Give the extent of all Plasmodium falciparum-infected red blood cells.
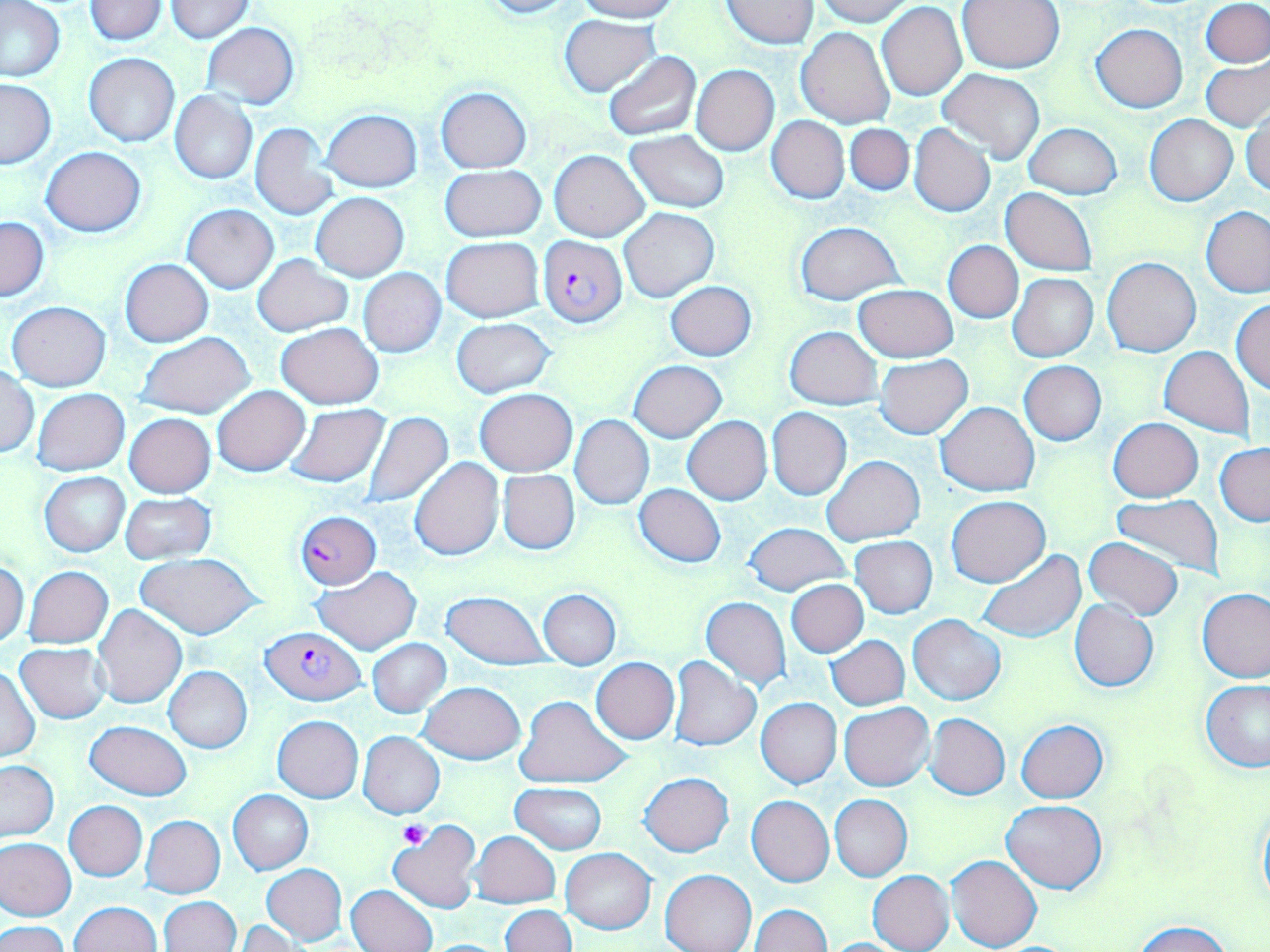
Approximate bounding boxes as (x1, y1, x2, y2) in pixels.
Plasmodium falciparum-infected red blood cells: (537, 234, 626, 327), (295, 511, 379, 588), (261, 626, 365, 705).

Platelet locations: (398, 821, 429, 848). Uninfected red blood cell locations: (0, 0, 68, 83), (475, 0, 584, 19), (575, 0, 681, 22), (815, 0, 917, 26), (84, 1, 166, 44), (721, 1, 818, 49), (957, 1, 1065, 74), (1202, 1, 1269, 66), (164, 2, 254, 43), (878, 3, 967, 100), (560, 15, 658, 95), (201, 22, 299, 109), (1090, 22, 1188, 113), (796, 26, 896, 128), (602, 51, 701, 140), (84, 53, 179, 147), (1202, 59, 1270, 132), (690, 65, 779, 155), (937, 68, 1045, 164), (0, 78, 56, 168), (436, 86, 532, 172), (169, 91, 257, 184), (322, 108, 422, 193), (1243, 108, 1270, 199), (1145, 114, 1237, 205), (768, 115, 849, 203), (250, 123, 340, 219), (845, 123, 914, 195), (909, 123, 995, 218), (1023, 123, 1122, 199), (624, 131, 730, 211), (40, 146, 147, 236), (549, 148, 649, 241), (440, 166, 545, 243), (1002, 188, 1097, 275), (311, 193, 408, 281), (183, 204, 278, 293), (1202, 207, 1269, 296), (619, 208, 718, 301), (1, 217, 48, 301), (794, 221, 905, 304), (441, 237, 545, 323), (943, 241, 1023, 323), (253, 254, 352, 336), (1102, 256, 1200, 357), (120, 258, 213, 345), (358, 269, 447, 357), (1007, 273, 1098, 362), (665, 281, 756, 360), (853, 283, 958, 362), (800, 297, 954, 385), (1231, 299, 1270, 394), (7, 302, 111, 390), (450, 317, 557, 399), (277, 323, 383, 409), (785, 327, 882, 408), (136, 331, 256, 420), (1160, 346, 1255, 438), (875, 355, 973, 439), (630, 359, 726, 442), (1020, 360, 1107, 445), (1, 366, 40, 458), (212, 386, 309, 475), (32, 388, 129, 475), (475, 389, 576, 476), (936, 400, 1039, 496), (284, 403, 390, 487), (767, 407, 852, 501), (362, 411, 454, 507), (125, 413, 216, 497), (570, 415, 654, 509), (682, 416, 771, 504), (1108, 417, 1203, 502), (1215, 443, 1270, 525), (821, 455, 924, 547), (409, 457, 503, 561), (497, 470, 579, 555), (39, 472, 129, 556), (634, 484, 726, 567), (120, 492, 216, 564), (1110, 495, 1224, 578), (947, 496, 1049, 587), (744, 522, 850, 597), (851, 536, 937, 618), (1084, 536, 1183, 620), (977, 548, 1085, 643), (138, 554, 262, 640), (0, 560, 27, 647), (23, 566, 112, 649), (311, 566, 420, 654), (786, 580, 868, 657), (1198, 589, 1270, 684), (538, 590, 620, 669), (439, 591, 553, 670), (700, 597, 792, 690), (1069, 601, 1158, 691), (93, 604, 185, 709), (909, 614, 1004, 706), (826, 635, 910, 710), (367, 639, 452, 718), (15, 643, 110, 723), (666, 656, 762, 751), (592, 657, 679, 745), (1, 665, 40, 761), (164, 666, 252, 753), (1201, 680, 1270, 772), (417, 681, 525, 764), (514, 694, 631, 789), (756, 697, 842, 788), (839, 702, 933, 790), (518, 712, 623, 856), (925, 713, 1010, 800), (272, 715, 363, 802), (1016, 719, 1109, 803), (85, 720, 191, 800), (358, 731, 444, 819), (0, 759, 58, 842), (639, 773, 733, 856), (510, 782, 607, 855), (228, 789, 314, 875), (829, 794, 912, 881), (747, 796, 834, 887), (1256, 798, 1270, 913), (64, 800, 147, 881), (1002, 800, 1107, 892), (141, 815, 225, 897), (388, 820, 481, 914), (470, 832, 560, 908), (0, 837, 75, 920), (561, 848, 656, 934), (947, 854, 1041, 952), (262, 864, 347, 944), (660, 869, 756, 952), (867, 870, 954, 952), (347, 884, 437, 952), (159, 896, 240, 951), (69, 901, 162, 952), (500, 904, 575, 952), (749, 904, 831, 952), (234, 920, 305, 951), (1131, 920, 1232, 952), (0, 921, 69, 952), (819, 938, 915, 951). Slide-level diagnosis: Plasmodium falciparum. Single field of view. Optical microscopy. May-Grünwald-Giemsa-stained preparation. 1000x magnification. Image is 1270×952 pixels. Thin blood smear.